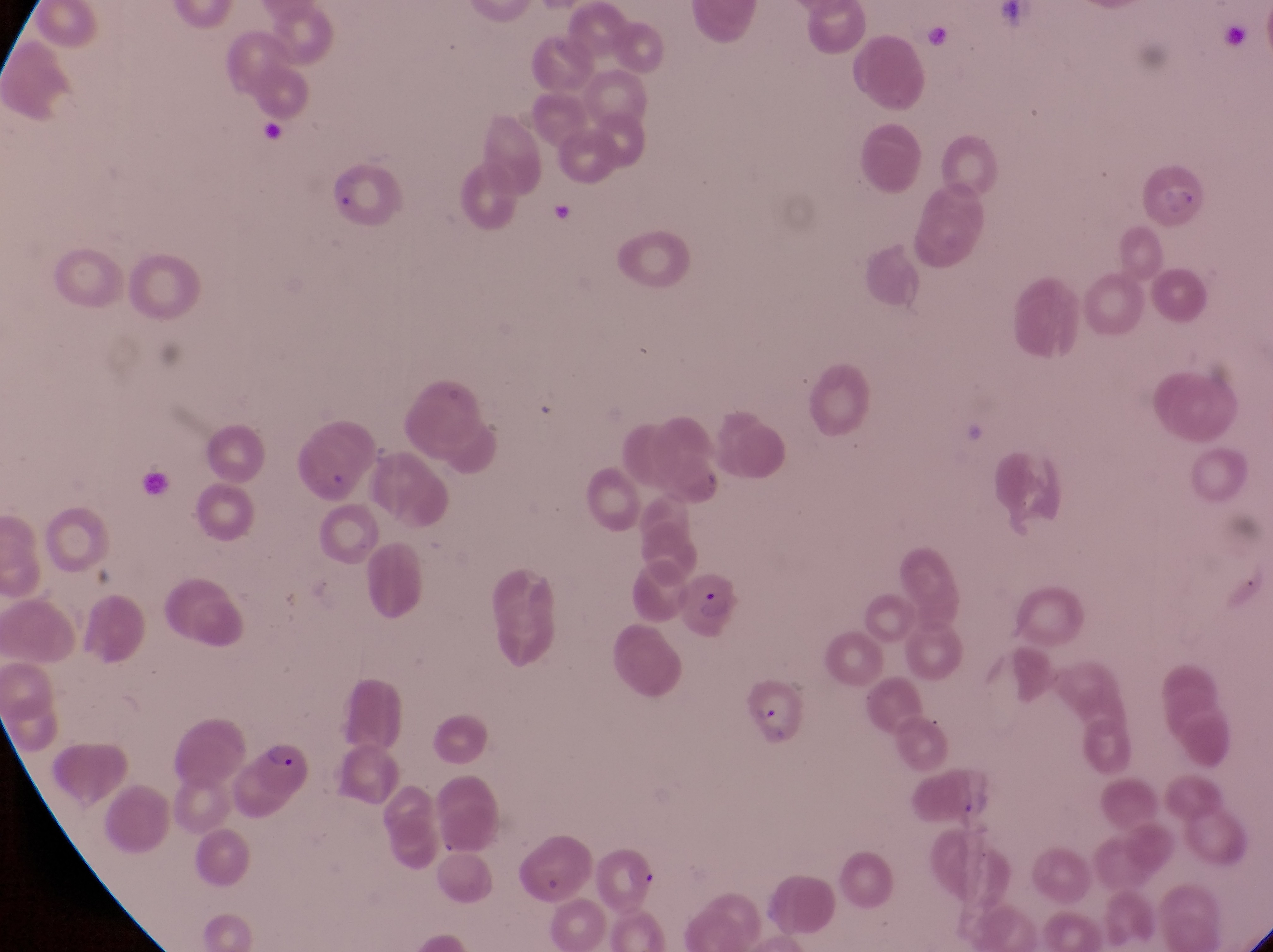
Approximate bounding boxes as (left, top, right, bottom) in pixels.
Summary:
  - Parasitised red blood cell locations: (325, 153, 407, 231), (672, 572, 737, 639), (747, 675, 805, 745), (237, 742, 319, 820)
  - Country: Uganda
  - Capture: smartphone photograph through the eyepiece of an Olympus CX-23 microscope
  - Image size: 1273×952 pixels
  - Field of view: single
  - Magnification: 1000x
  - Preparation: thin blood film